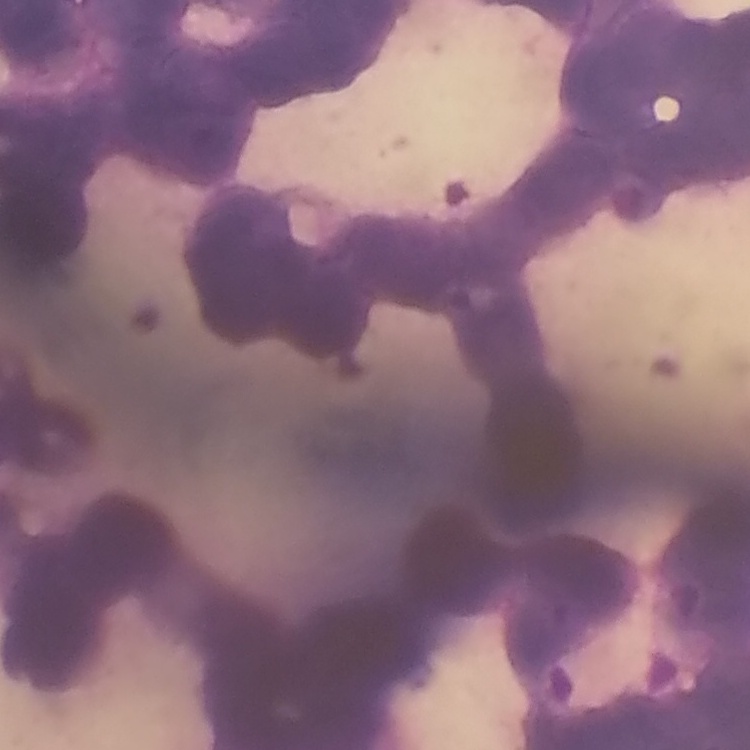

The red blood cells exhibit rouleaux formation. Thin peripheral smear. One tile cut from a larger photomicrograph. Field's or Giemsa stain.